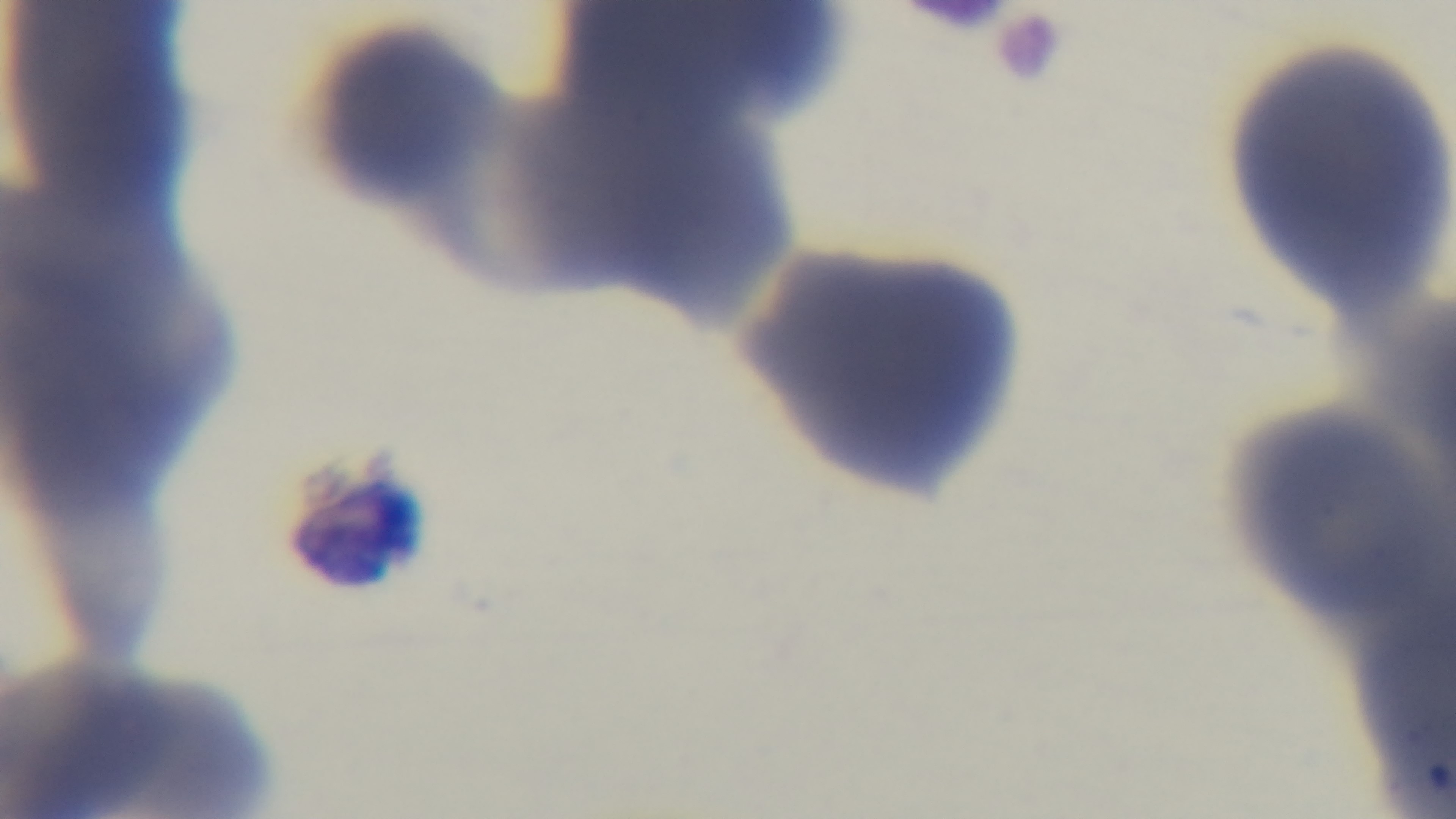
Summary:
  - Capture: mounted 4K digital camera
  - Malaria status: negative
  - Objective: 100x oil immersion
  - Preparation: thin smear
  - Modality: light microscopy
  - Stain: Giemsa
  - Field of view: one from the slide